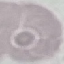

{
  "result": "negative for malaria parasites",
  "image_type": "automatically extracted cell patch, resized to 64 × 64 pixels",
  "capture": "smartphone through the microscope eyepiece",
  "preparation": "thin blood smear",
  "stain": "Giemsa"
}